Assess the morphology of the red blood cells.
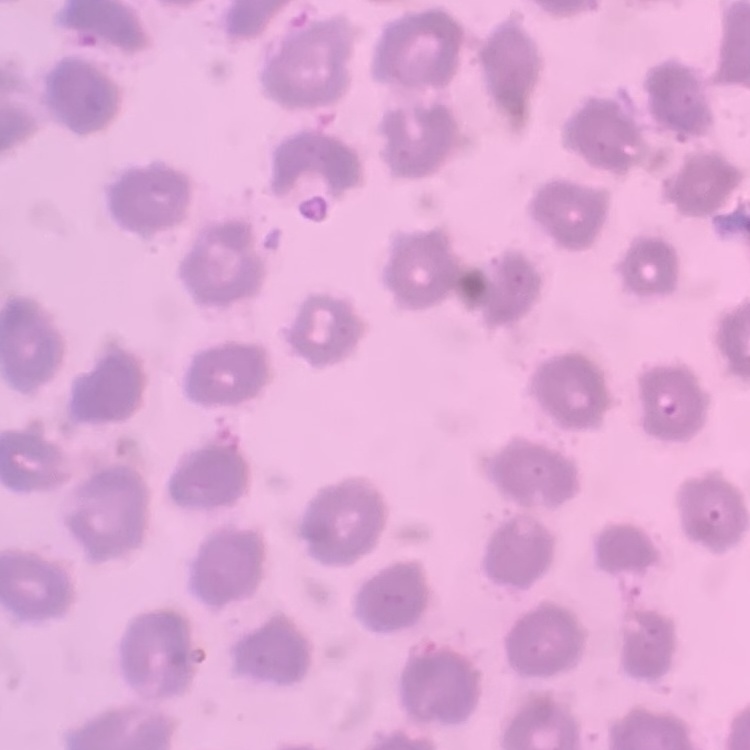

They show no rouleaux formation.

Thin blood film. Stained with either Field's or Giemsa. One tile cut from a larger photomicrograph.